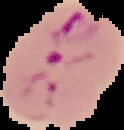

preparation = thin blood film
result = Plasmodium parasites detected
image size = 124×130 pixels
image type = segmented cell region on a black background